Outline each P. falciparum parasite and classify it by life-cycle stage.
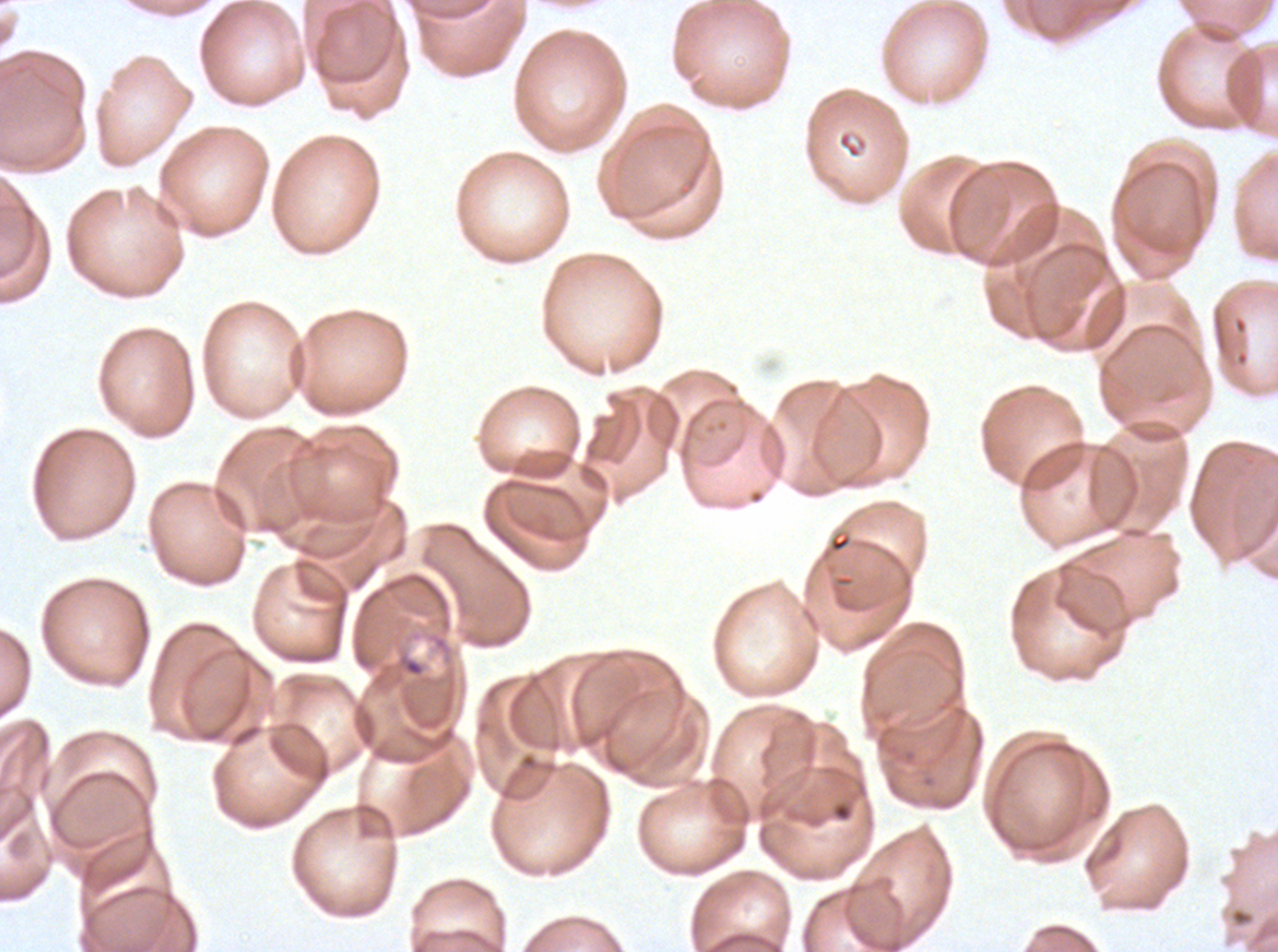
No rings, late-ring/early-trophozoite forms, mid trophozoites, late trophozoites, early schizonts, late schizonts, segmenters, or gametocytes observed.

Approximate bounding rectangles given as corner coordinates in pixels from the top-left. Debris locations: (x1=397, y1=653, x2=425, y2=677), (x1=829, y1=799, x2=855, y2=824). Giemsa stain. Thin blood film. A sub-image separated from a larger composite. Image is 1278×952 pixels. P. falciparum cultured ex vivo for 24 to 48 hours, from a patient in The Gambia.